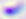
Summary:
  - Identification: Toxoplasma gondii
  - Magnification: 400x
  - Modality: micrograph